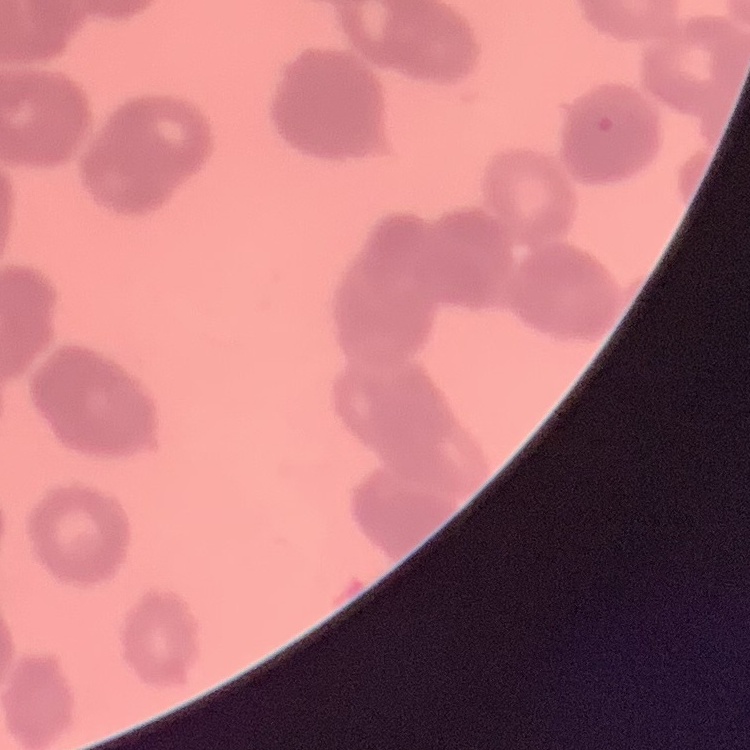 The red blood cells exhibit rouleaux formation. Square crop of a larger photomicrograph. Thin peripheral smear. Field's or Giemsa stain.